Outline each blood parasite and name the species.
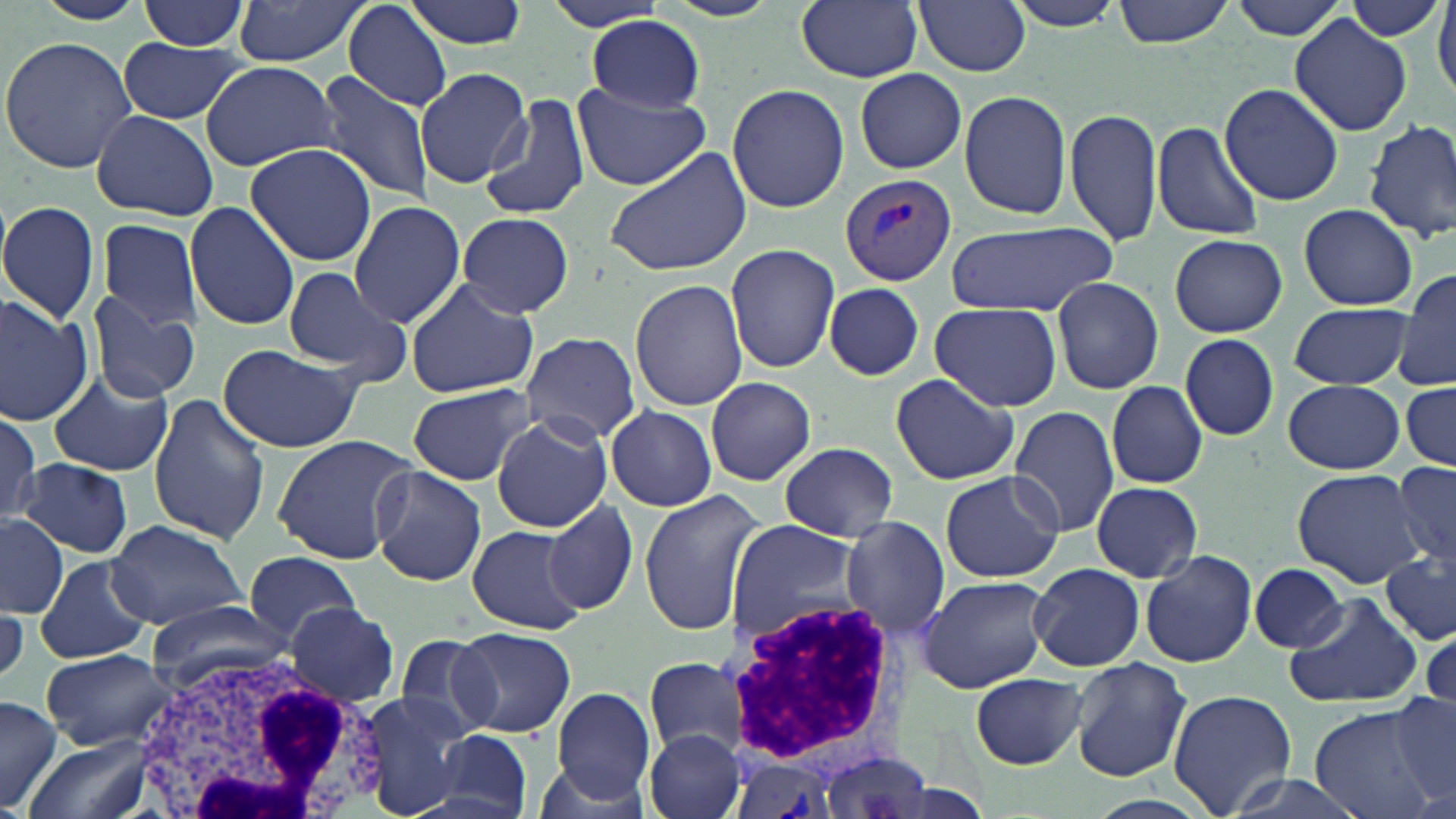
Approximate bounding boxes as (x1, y1, x2, y2) in pixels.
Plasmodium vivax-infected red blood cells: (840, 175, 959, 287), (728, 754, 847, 819).
No Plasmodium falciparum, Plasmodium ovale, Plasmodium malariae, Babesia divergens, or Trypanosoma brucei observed.

Uninfected red blood cell locations: (232, 0, 370, 66), (406, 0, 528, 49), (797, 0, 923, 82), (1004, 0, 1130, 32), (1113, 0, 1235, 46), (1228, 0, 1355, 40), (1433, 0, 1455, 102), (33, 1, 148, 27), (138, 1, 253, 51), (538, 1, 675, 33), (914, 1, 1031, 76), (1345, 1, 1442, 43), (345, 2, 452, 111), (1290, 14, 1415, 137), (590, 17, 706, 112), (0, 36, 140, 174), (117, 37, 250, 123), (200, 61, 340, 170), (415, 67, 534, 190), (854, 70, 966, 173), (312, 71, 437, 204), (576, 82, 713, 190), (726, 83, 849, 213), (1220, 83, 1347, 207), (958, 90, 1071, 219), (481, 92, 591, 221), (1066, 105, 1163, 247), (90, 109, 220, 221), (1365, 119, 1456, 245), (1152, 120, 1266, 242), (244, 142, 376, 267), (604, 146, 753, 277), (0, 200, 101, 326), (349, 200, 467, 328), (186, 202, 300, 330), (1296, 206, 1417, 310), (456, 212, 575, 318), (98, 218, 205, 330), (945, 221, 1116, 315), (1170, 235, 1286, 338), (725, 242, 838, 373), (281, 267, 412, 380), (1395, 270, 1456, 392), (402, 278, 541, 400), (629, 278, 748, 410), (1051, 278, 1163, 393), (824, 281, 924, 381), (91, 295, 199, 403), (0, 296, 93, 427), (929, 301, 1061, 412), (1288, 302, 1412, 389), (519, 331, 643, 445), (1179, 333, 1280, 441), (216, 345, 364, 454), (48, 370, 173, 477), (891, 374, 1020, 487), (705, 377, 815, 485), (1285, 380, 1404, 474), (1400, 380, 1456, 472), (408, 381, 535, 486), (1106, 382, 1207, 489), (148, 394, 271, 546), (605, 404, 718, 511), (1009, 405, 1121, 539), (1, 409, 43, 523), (492, 413, 613, 532), (272, 434, 417, 565), (778, 442, 899, 539), (20, 457, 133, 558), (1393, 462, 1455, 568), (369, 468, 489, 587), (1292, 468, 1428, 587), (941, 472, 1062, 583), (1091, 481, 1203, 581), (639, 489, 763, 635), (543, 500, 640, 616), (0, 514, 67, 615), (841, 516, 949, 639), (106, 518, 247, 631), (730, 523, 864, 642), (467, 525, 589, 634), (1141, 548, 1258, 667), (1380, 551, 1455, 645), (241, 553, 364, 644), (34, 554, 153, 665), (1028, 562, 1142, 672), (1250, 563, 1348, 653), (918, 575, 1051, 693), (1282, 589, 1425, 710), (0, 600, 26, 687), (147, 601, 292, 684), (282, 602, 401, 704), (451, 627, 576, 737), (395, 633, 498, 736), (1421, 635, 1456, 710), (41, 648, 173, 749), (643, 656, 747, 761), (1071, 657, 1193, 782), (970, 673, 1086, 768), (553, 688, 656, 800), (1167, 688, 1297, 816), (1387, 690, 1455, 810), (359, 691, 470, 817), (0, 692, 62, 813), (1308, 703, 1443, 819), (644, 728, 747, 819), (430, 730, 533, 818), (27, 737, 153, 819), (1217, 771, 1370, 819). White blood cell locations: (723, 600, 899, 778), (123, 651, 377, 817). Slide-level diagnosis: Plasmodium vivax. Captured at 1000x magnification. Optical microscopy. One field of a larger specimen. May-Grünwald-Giemsa-stained preparation. Image is 1456×819 pixels. Thin blood smear.